Assess this cell for malaria.
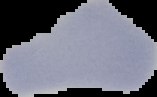
It is uninfected.

Cell region segmented out of the field of view; the surrounding area is masked to black. Image is 157×97 pixels. From a thin blood smear.